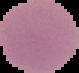
Result: no malaria parasites seen. Image is 79×73 pixels. From a thin blood film. Cell region segmented out of the field of view; the surrounding area is masked to black.